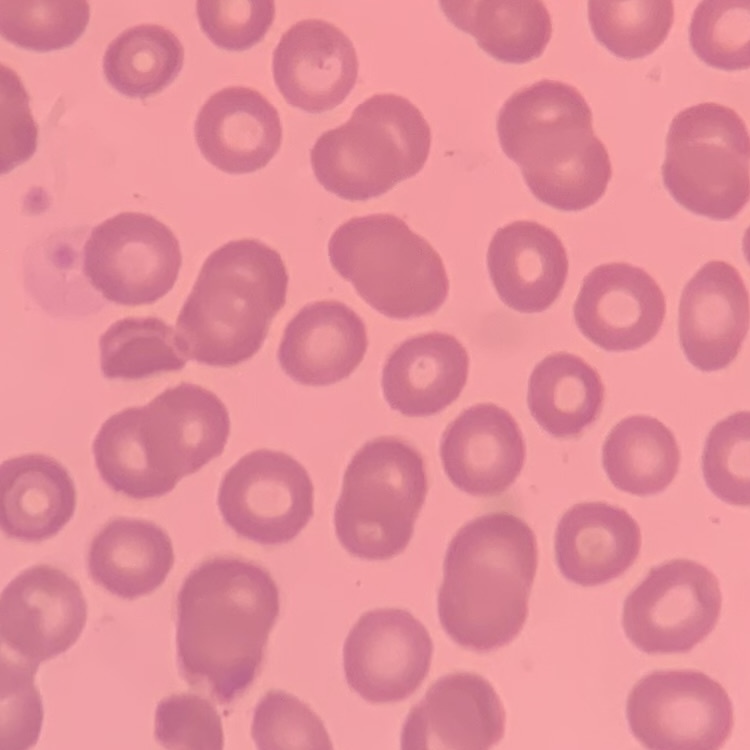
The red blood cells show no rouleaux formation. Field's or Giemsa stain. One tile cut from a larger photomicrograph. Thin peripheral smear.